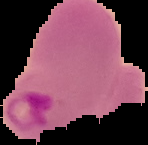
{
  "image_size": "148×145 pixels",
  "malaria_status": "parasitized",
  "preparation": "thin blood film",
  "image_type": "cell region segmented out of the field of view; surrounding area masked to black"
}